Name the cell type shown.
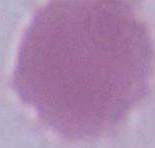

This is an erythrocyte.

Summary:
  - Modality: photomicrograph
  - Magnification: 1000x